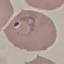 Result: malaria parasites identified. Thin smear of blood. Giemsa-stained preparation. Photographed with a smartphone camera at the microscope eyepiece. Cell patch, automatically extracted from a larger field of view and resized to 64 × 64 pixels.